Identify the parasite.
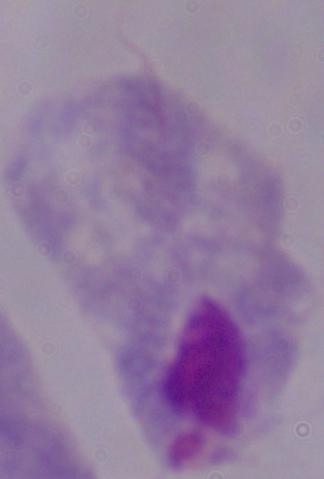
A trichomonad.

Summary:
  - Modality: micrograph
  - Magnification: 1000x